Classify this cell by malaria status.
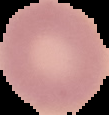

Uninfected.

image_type: segmented cell region on a black background
preparation: thin blood film
image_size: 109×115 pixels